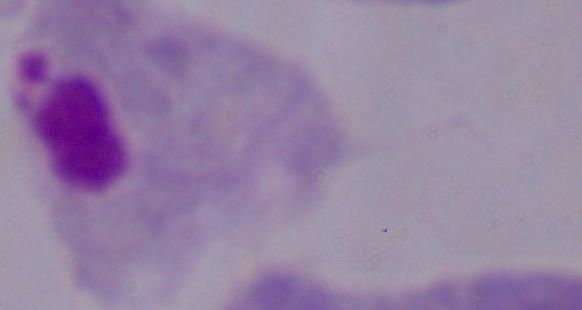

{
  "modality": "micrograph",
  "magnification": "1000x",
  "identification": "trichomonad"
}